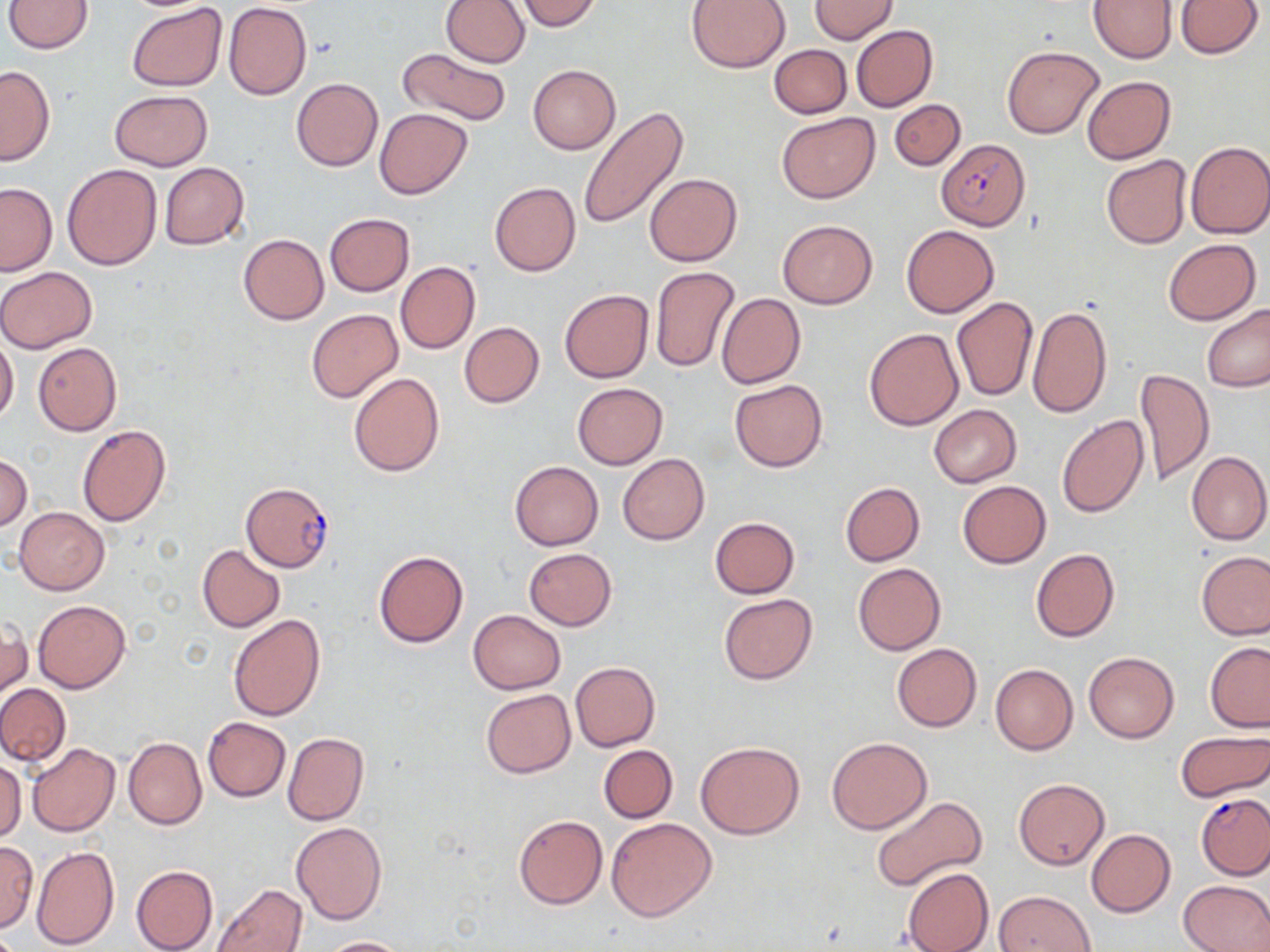

Approximate bounding boxes as (x1, y1, x2, y2) in pixels. Plasmodium falciparum-infected red blood cell locations: (936, 139, 1030, 229), (241, 482, 334, 572), (1196, 794, 1270, 879). Uninfected red blood cell locations: (4, 0, 94, 53), (440, 0, 531, 67), (514, 0, 602, 32), (686, 0, 792, 72), (809, 0, 898, 43), (1175, 0, 1263, 58), (1088, 1, 1176, 63), (223, 2, 311, 100), (127, 4, 227, 92), (851, 25, 937, 112), (769, 44, 852, 119), (1002, 46, 1103, 137), (397, 47, 512, 127), (385, 51, 498, 193), (529, 64, 620, 153), (0, 65, 55, 165), (1081, 76, 1176, 164), (291, 77, 383, 171), (109, 89, 212, 170), (889, 99, 965, 170), (577, 105, 689, 227), (375, 108, 472, 198), (776, 113, 879, 203), (1185, 141, 1270, 239), (1101, 154, 1192, 249), (159, 162, 249, 249), (62, 163, 162, 270), (643, 173, 742, 265), (489, 181, 581, 276), (0, 183, 56, 275), (325, 213, 414, 295), (777, 220, 878, 309), (902, 224, 999, 318), (238, 234, 329, 325), (1163, 238, 1261, 325), (395, 262, 480, 354), (651, 266, 739, 372), (0, 267, 99, 354), (559, 289, 653, 383), (717, 293, 805, 389), (952, 296, 1038, 400), (1202, 304, 1270, 392), (1028, 305, 1113, 418), (306, 308, 403, 403), (459, 322, 544, 407), (864, 327, 964, 430), (0, 333, 18, 428), (33, 343, 121, 436), (1135, 368, 1213, 486), (349, 371, 445, 477), (730, 379, 828, 472), (572, 382, 667, 469), (927, 405, 1021, 488), (1056, 415, 1150, 519), (77, 425, 171, 527), (1185, 450, 1270, 545), (0, 453, 31, 532), (617, 454, 709, 545), (510, 462, 604, 550), (957, 480, 1050, 567), (840, 481, 925, 565), (14, 506, 110, 595), (710, 516, 800, 598), (197, 544, 286, 632), (524, 548, 615, 629), (1030, 548, 1120, 643), (374, 550, 468, 647), (1195, 551, 1269, 639), (853, 562, 945, 655), (718, 593, 818, 685), (32, 600, 130, 692), (467, 610, 566, 694), (228, 614, 326, 722), (1, 618, 31, 703), (1204, 642, 1270, 733), (892, 643, 982, 731), (1084, 652, 1179, 743), (571, 661, 659, 751), (991, 664, 1078, 755), (0, 684, 71, 767), (480, 688, 575, 778), (202, 717, 291, 801), (1176, 730, 1270, 801), (283, 732, 368, 826), (123, 736, 207, 830), (826, 737, 931, 834), (696, 741, 804, 839), (26, 744, 119, 836), (598, 745, 678, 823), (1, 759, 25, 843), (1014, 779, 1109, 868), (871, 796, 986, 892), (513, 813, 607, 910), (607, 816, 717, 921), (291, 821, 387, 925), (1086, 829, 1175, 917), (0, 839, 38, 931), (30, 845, 120, 949), (130, 865, 218, 952), (902, 867, 994, 952), (1179, 879, 1270, 952), (212, 883, 306, 952), (995, 890, 1094, 952), (318, 937, 410, 952). Slide-level diagnosis: Plasmodium falciparum. May-Grünwald-Giemsa-stained preparation. Thin blood smear. Captured at 1000x magnification. Single field of view. Optical microscopy. Image is 1270×952 pixels.